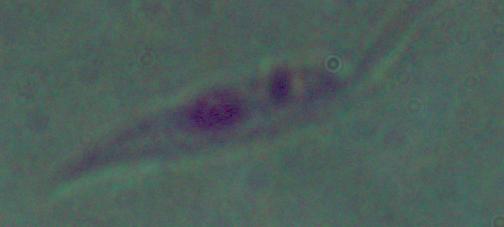 A Leishmania parasite is seen. Micrograph. Captured at 1000x magnification.